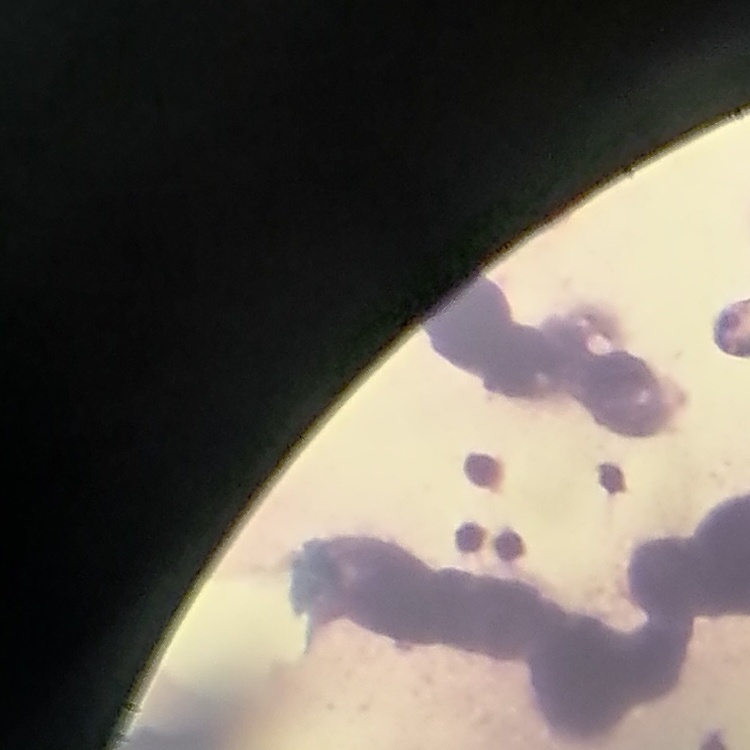

Summary:
  - Red blood cell morphology: rouleaux formation
  - Stain: Field's or Giemsa
  - Image type: one tile cut from a larger photomicrograph
  - Preparation: thin blood smear